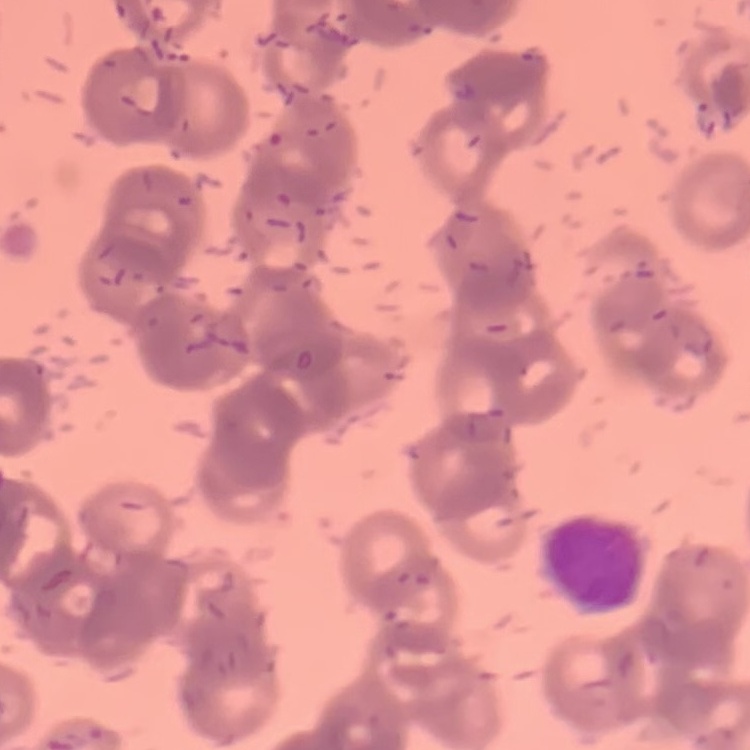

Summary:
  - Erythrocyte morphology: rouleaux formation
  - Image type: square crop of a larger photomicrograph
  - Preparation: thin blood film
  - Stain: Field's or Giemsa